State the blood parasite species.
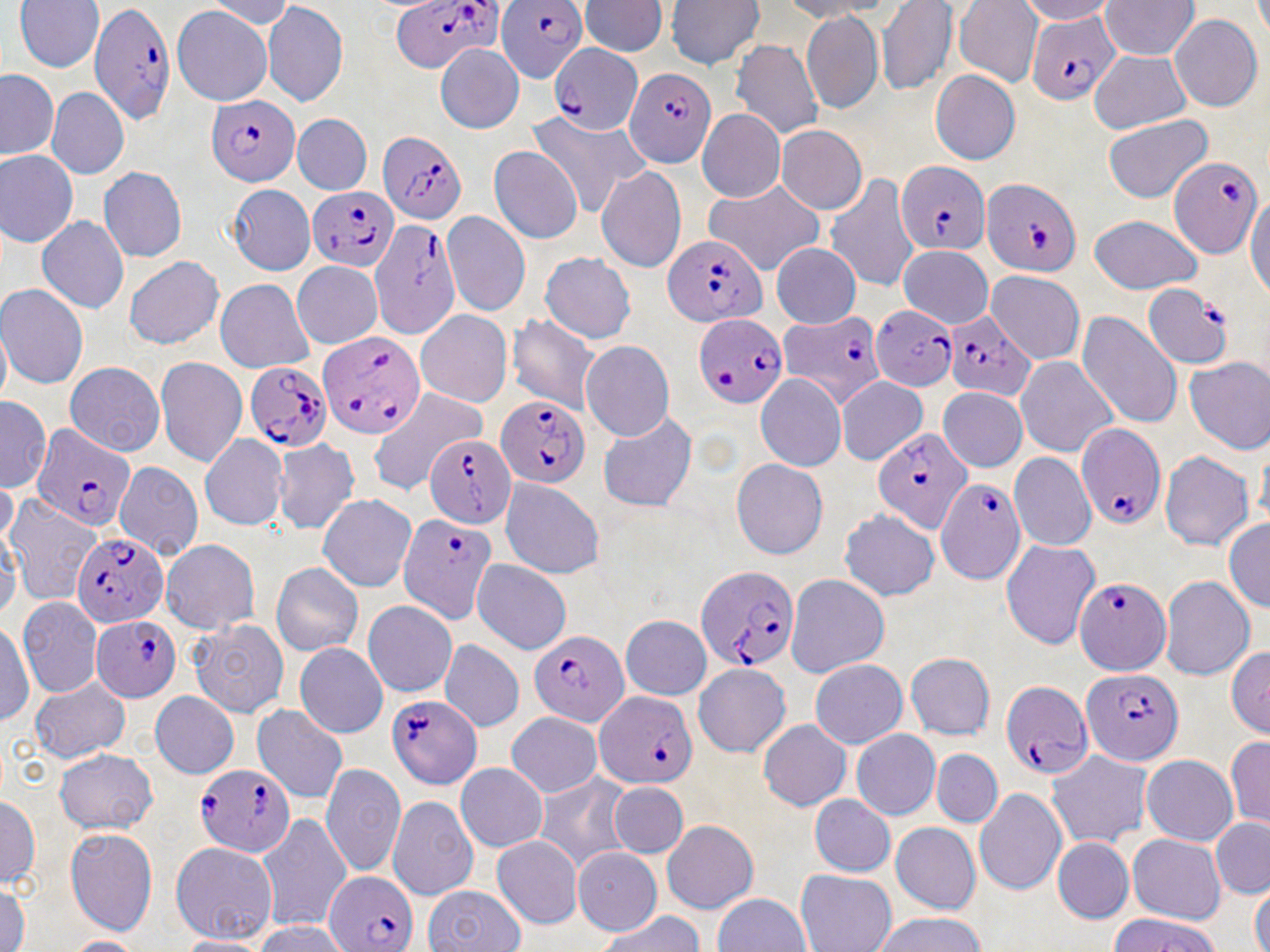

Plasmodium falciparum.

field of view = single
Plasmodium falciparum-infected red blood cell locations = approximate bounding boxes as (x1,y1)-(x2,y2) corner pairs in pixels: (499,0)-(588,81), (383,2)-(507,68), (91,4)-(180,121), (1023,10)-(1113,106), (550,41)-(642,135), (627,67)-(717,167), (204,98)-(302,186), (379,130)-(470,228), (1169,157)-(1260,255), (896,162)-(990,252), (986,174)-(1081,274), (305,187)-(395,272), (372,222)-(456,336), (658,230)-(769,324), (1142,285)-(1230,367), (873,303)-(955,391), (950,313)-(1035,401), (695,314)-(788,410), (780,314)-(881,408), (318,334)-(422,438), (246,364)-(332,452), (497,401)-(586,488), (35,426)-(133,527), (1079,426)-(1163,528), (875,431)-(972,535), (422,434)-(513,523), (938,479)-(1023,584), (400,517)-(494,624), (70,529)-(165,621), (696,564)-(801,676), (1075,575)-(1171,672), (93,612)-(184,700), (527,628)-(627,721), (1078,668)-(1186,765), (1003,679)-(1092,783), (382,689)-(482,793), (595,689)-(696,792), (191,759)-(299,854), (323,868)-(424,950)
magnification = 1000x
uninfected red blood cell locations = approximate bounding boxes as (x1,y1)-(x2,y2) corner pairs in pixels: (4,0)-(99,71), (587,1)-(670,58), (672,1)-(762,69), (957,1)-(1039,84), (262,2)-(350,103), (1104,3)-(1199,59), (876,4)-(952,92), (170,6)-(272,104), (806,9)-(884,115), (1174,13)-(1260,109), (734,40)-(823,133), (438,41)-(523,133), (1088,57)-(1190,135), (930,67)-(1019,162), (45,84)-(123,179), (700,106)-(782,203), (295,109)-(370,190), (526,112)-(648,214), (294,114)-(370,193), (1103,116)-(1212,204), (781,128)-(864,214), (0,145)-(69,250), (492,149)-(583,242), (100,165)-(185,259), (597,165)-(687,272), (826,174)-(917,290), (223,182)-(316,273), (702,183)-(823,273), (219,186)-(317,275), (443,214)-(528,315), (1091,216)-(1201,296), (39,217)-(128,311), (774,245)-(855,329), (902,245)-(991,327), (540,249)-(637,348), (122,255)-(226,351), (294,262)-(382,348), (985,273)-(1079,363), (2,280)-(85,389), (217,280)-(313,372), (1078,312)-(1181,425), (416,313)-(511,409), (507,316)-(600,416), (583,343)-(671,441), (156,357)-(245,464), (1185,357)-(1270,451), (62,359)-(161,459), (1017,360)-(1117,458), (758,375)-(845,470), (840,380)-(924,465), (938,390)-(1025,469), (369,391)-(485,495), (600,416)-(695,511), (202,433)-(286,531), (279,440)-(356,533), (1160,451)-(1251,554), (1011,452)-(1098,548), (116,461)-(203,560), (733,461)-(823,558), (504,476)-(601,578), (319,498)-(415,592), (841,510)-(937,602), (158,536)-(261,635), (1000,544)-(1098,647), (473,561)-(568,653), (271,565)-(363,653), (1161,573)-(1251,677), (785,578)-(883,678), (19,596)-(98,697), (365,602)-(454,698), (188,612)-(288,716), (625,617)-(712,699), (295,641)-(387,736), (437,641)-(526,731), (1231,642)-(1268,738), (905,648)-(997,742), (695,660)-(787,760), (811,660)-(904,748), (27,681)-(131,758), (150,692)-(236,780), (253,707)-(347,802), (507,713)-(604,796), (760,720)-(848,814), (852,729)-(937,819), (1226,738)-(1270,823), (53,747)-(157,834), (1045,749)-(1147,847), (932,751)-(1000,826), (1141,751)-(1238,843), (322,766)-(404,876), (456,767)-(547,851), (540,775)-(623,865), (613,784)-(684,858), (974,789)-(1064,890), (391,790)-(476,897), (3,792)-(41,889), (811,797)-(894,873), (258,815)-(351,927), (663,819)-(756,913), (892,820)-(980,914), (1212,821)-(1270,899), (67,827)-(156,931), (493,834)-(579,927), (1128,836)-(1223,923), (1053,837)-(1130,922), (172,843)-(276,943), (575,849)-(660,936), (798,871)-(892,952), (428,886)-(522,952), (713,895)-(809,952), (1100,913)-(1232,952), (880,915)-(983,952)
preparation = thin blood smear
modality = light microscopy
stain = May-Grünwald-Giemsa
image size = 1270×952 pixels